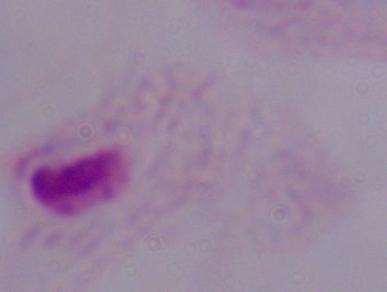 Photomicrograph. Captured at 1000x magnification. A trichomonad is seen.